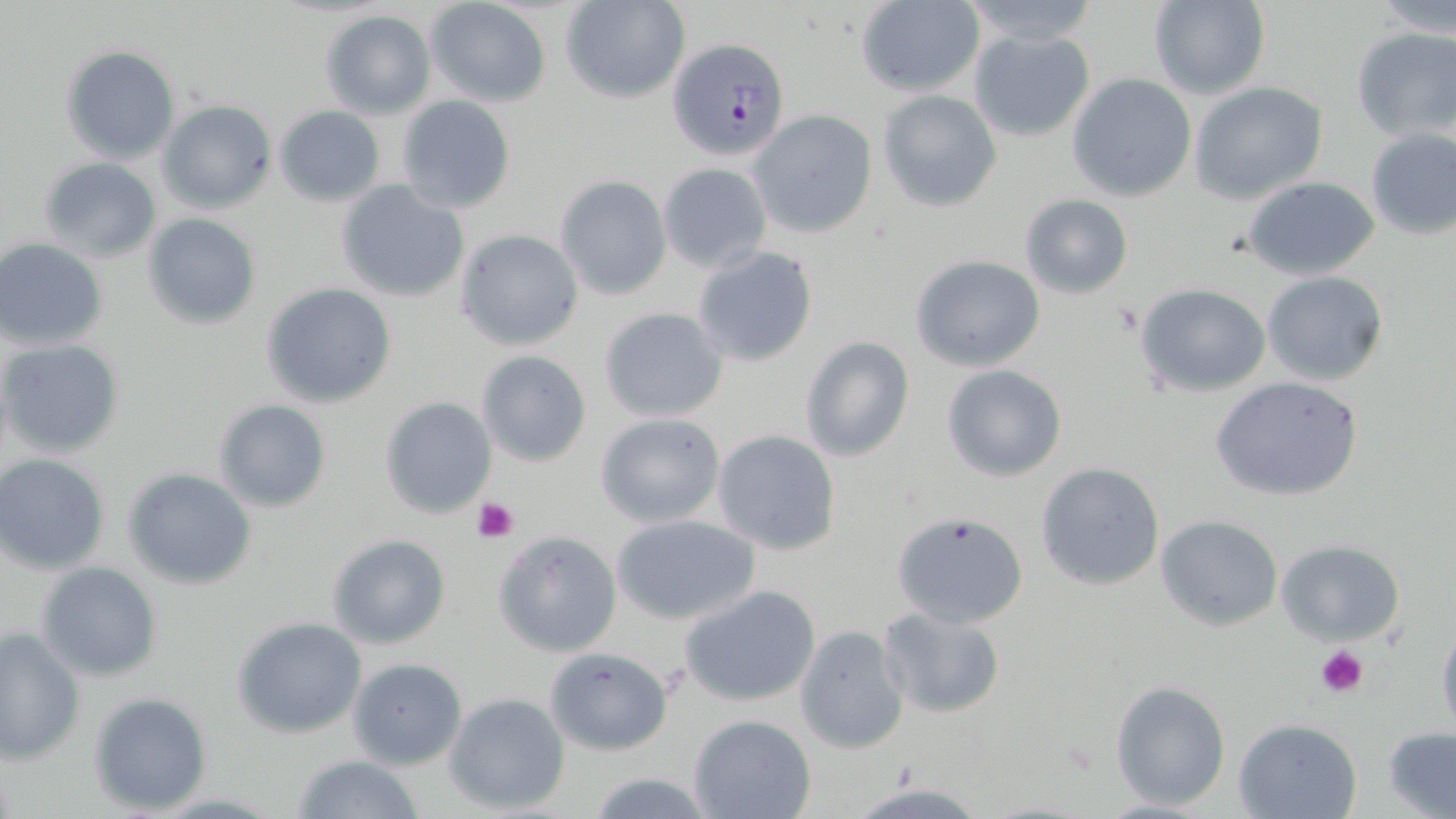

Approximate bounding boxes as [x1, y1, x2, y2] in pixels. Platelet locations: [472, 498, 518, 543], [1315, 644, 1369, 698]. Plasmodium falciparum-infected red blood cell locations: [667, 37, 791, 160]. Uninfected red blood cell locations: [563, 0, 690, 103], [1148, 0, 1270, 100], [1372, 0, 1456, 38], [426, 1, 552, 107], [853, 1, 986, 98], [958, 1, 1103, 49], [319, 10, 436, 118], [1351, 26, 1456, 142], [968, 28, 1095, 141], [60, 45, 181, 163], [1066, 73, 1198, 202], [1190, 82, 1329, 203], [877, 89, 1001, 212], [395, 95, 516, 214], [156, 100, 278, 215], [273, 104, 386, 207], [749, 109, 878, 239], [1363, 126, 1456, 240], [38, 157, 162, 263], [658, 161, 771, 273], [555, 175, 671, 299], [1242, 175, 1382, 281], [335, 180, 470, 304], [1019, 194, 1133, 299], [142, 213, 261, 329], [455, 228, 584, 351], [2, 238, 110, 349], [691, 244, 820, 369], [909, 253, 1045, 371], [1263, 271, 1388, 386], [262, 283, 396, 407], [1135, 283, 1272, 397], [598, 306, 729, 422], [799, 335, 917, 463], [0, 337, 125, 460], [475, 351, 592, 466], [941, 364, 1067, 482], [1209, 375, 1365, 502], [377, 396, 497, 519], [213, 400, 332, 514], [594, 412, 727, 528], [712, 428, 842, 556], [1, 454, 114, 573], [1035, 461, 1165, 591], [123, 467, 257, 590], [891, 510, 1029, 628], [611, 513, 761, 625], [1156, 515, 1283, 632], [493, 530, 622, 658], [326, 533, 452, 649], [1274, 541, 1407, 645], [36, 561, 162, 681], [681, 585, 820, 708], [876, 607, 1005, 718], [1434, 613, 1456, 737], [232, 617, 368, 737], [794, 625, 910, 753], [0, 628, 85, 764], [543, 646, 673, 755], [347, 657, 468, 769], [1109, 679, 1232, 810], [89, 691, 212, 814], [444, 692, 571, 815], [688, 714, 817, 819], [1232, 717, 1363, 819], [1383, 726, 1456, 818], [291, 755, 427, 818], [585, 769, 715, 819], [845, 782, 991, 818]. Slide-level diagnosis: Plasmodium falciparum. May-Grünwald-Giemsa stain. Thin blood smear. Single field of view. Light microscopy. 1000x magnification. Image is 1456×819 pixels.